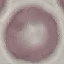
Result: no malaria parasites detected. Automatically extracted cell patch, resized to 64 × 64 pixels. Thin smear of blood. Photographed with a smartphone camera at the microscope eyepiece. Giemsa-stained preparation.